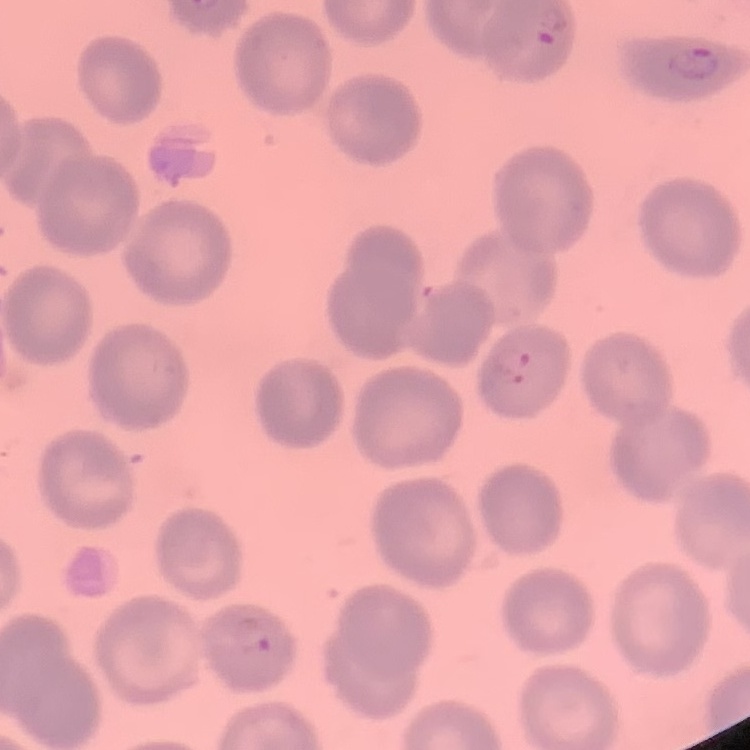

erythrocyte_morphology: no rouleaux formation
image_type: square crop of a larger photomicrograph
stain: Field's or Giemsa
preparation: thin blood film